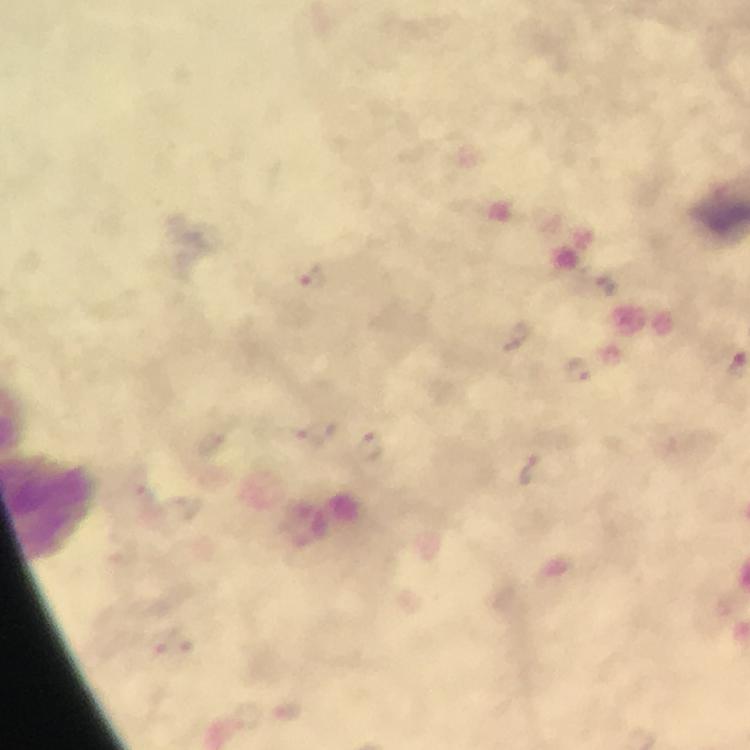
Approximate object centers, in pixels from the top-left corner.
Summary:
  - Malaria parasite locations: (x=312, y=276), (x=315, y=432), (x=370, y=444)
  - Immersion oil: applied
  - Cropped from: one field of view
  - Capture: smartphone mounted on the microscope
  - Magnification: 100x
  - Context: from a diagnostic examination for malaria
  - Stain: Giemsa
  - Preparation: thick blood smear
  - Image size: 750×750 pixels